Outline each Plasmodium vivax-infected red blood cell.
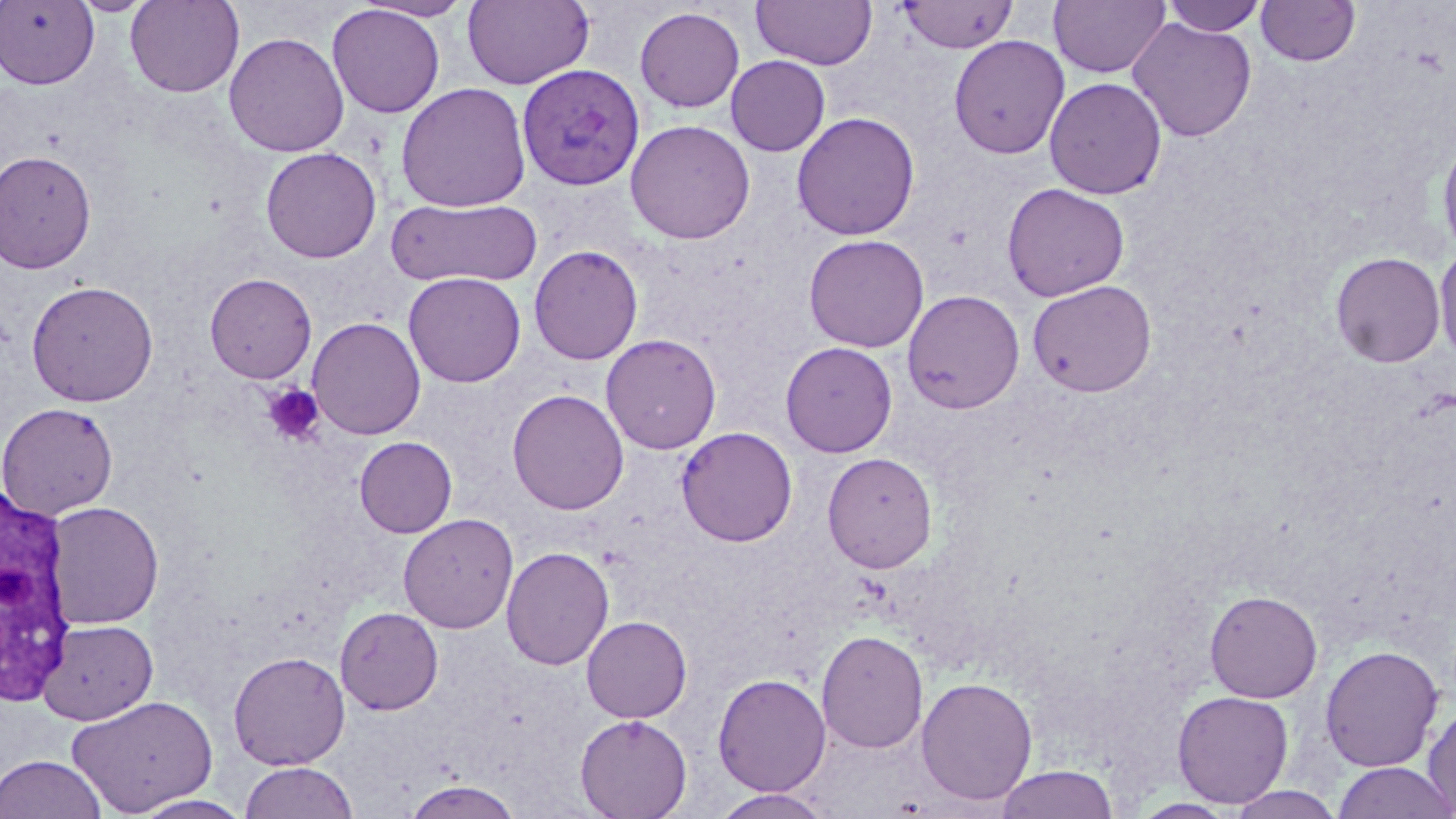

Approximate bounding boxes as (x1, y1, x2, y2) in pixels.
Plasmodium vivax-infected red blood cells: (517, 63, 645, 191).

Summary:
  - Uninfected red blood cell locations: (0, 0, 99, 90), (68, 0, 156, 16), (125, 0, 244, 97), (354, 0, 476, 21), (462, 0, 595, 90), (751, 0, 877, 70), (1049, 0, 1170, 79), (1161, 0, 1268, 37), (1256, 0, 1360, 67), (897, 1, 1018, 53), (327, 4, 445, 118), (634, 6, 745, 112), (1127, 17, 1257, 142), (224, 32, 349, 157), (949, 35, 1070, 159), (726, 55, 830, 156), (1044, 77, 1167, 199), (396, 82, 531, 212), (791, 111, 920, 240), (625, 119, 756, 244), (1437, 133, 1456, 260), (260, 147, 382, 263), (0, 149, 97, 273), (1002, 182, 1130, 301), (387, 197, 542, 287), (803, 234, 929, 352), (1434, 242, 1456, 364), (529, 244, 644, 365), (1330, 251, 1446, 368), (403, 272, 526, 387), (204, 273, 317, 383), (25, 279, 159, 407), (1027, 279, 1157, 397), (902, 290, 1024, 413), (307, 317, 426, 439), (600, 333, 722, 454), (780, 341, 898, 457), (507, 388, 629, 515), (0, 401, 119, 519), (676, 426, 797, 547), (354, 436, 457, 537), (822, 452, 937, 573), (44, 501, 164, 629), (398, 513, 519, 634), (501, 546, 614, 670), (1205, 590, 1322, 702), (334, 606, 444, 715), (581, 616, 692, 722), (37, 619, 157, 725), (816, 629, 928, 754), (1320, 644, 1444, 772), (228, 651, 350, 770), (712, 672, 831, 797), (916, 677, 1038, 804), (1172, 690, 1294, 807), (66, 694, 218, 816), (1423, 700, 1456, 817), (575, 714, 692, 818), (0, 753, 106, 819), (239, 761, 359, 819), (1332, 761, 1456, 819), (995, 765, 1119, 818), (401, 779, 524, 818), (1221, 785, 1346, 818), (710, 789, 835, 818), (129, 794, 255, 818)
  - White blood cell locations: (0, 485, 78, 711)
  - Platelet locations: (261, 383, 326, 446)
  - Slide-level diagnosis: Plasmodium vivax
  - Magnification: 1000x
  - Modality: optical microscopy
  - Field of view: one of a larger specimen
  - Preparation: thin blood film
  - Image size: 1456×819 pixels
  - Stain: May-Grünwald-Giemsa